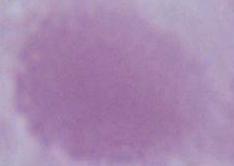
1000x magnification. A red blood cell is seen. Micrograph.